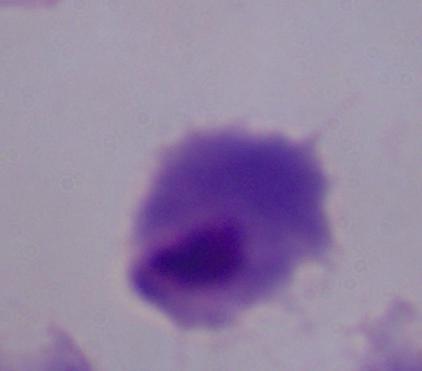
Summary:
  - Identification: trichomonad
  - Magnification: 1000x
  - Modality: micrograph